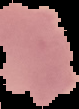

preparation: thin blood smear
image_size: 79×109 pixels
result: malaria parasites identified
image_type: segmented cell region with the area outside set to black